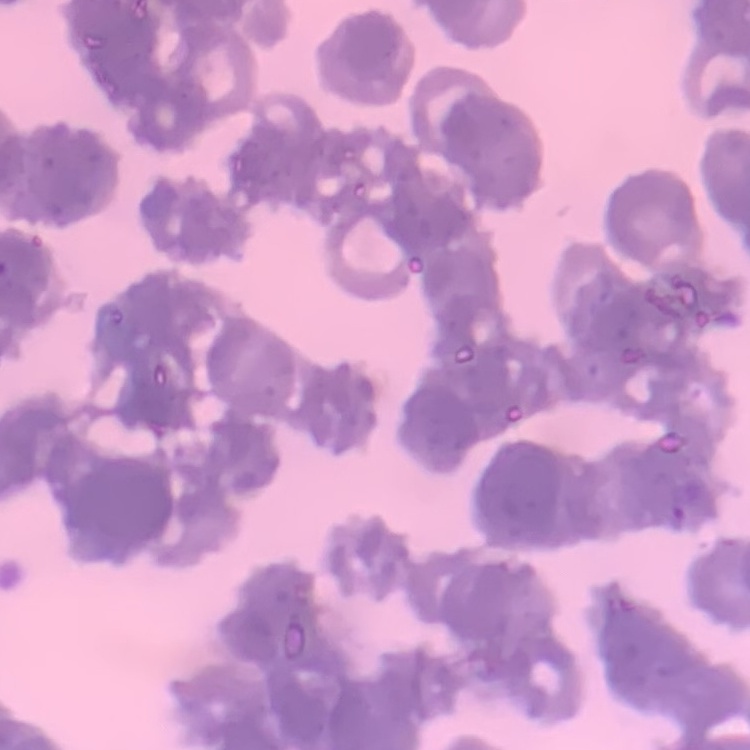 The erythrocytes exhibit rouleaux formation. Thin blood film. Field's or Giemsa stain. One tile cut from a larger photomicrograph.